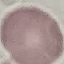

malaria status = uninfected
capture = smartphone camera at the microscope eyepiece
image type = automatically extracted cell patch, resized to 64 × 64 pixels
stain = Giemsa
preparation = thin blood smear